Classify this cell by malaria status.
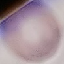

It is uninfected.

{
  "image_type": "automatically extracted cell patch, resized to 64 × 64 pixels",
  "preparation": "thin smear",
  "stain": "Giemsa",
  "capture": "smartphone camera at the microscope eyepiece"
}